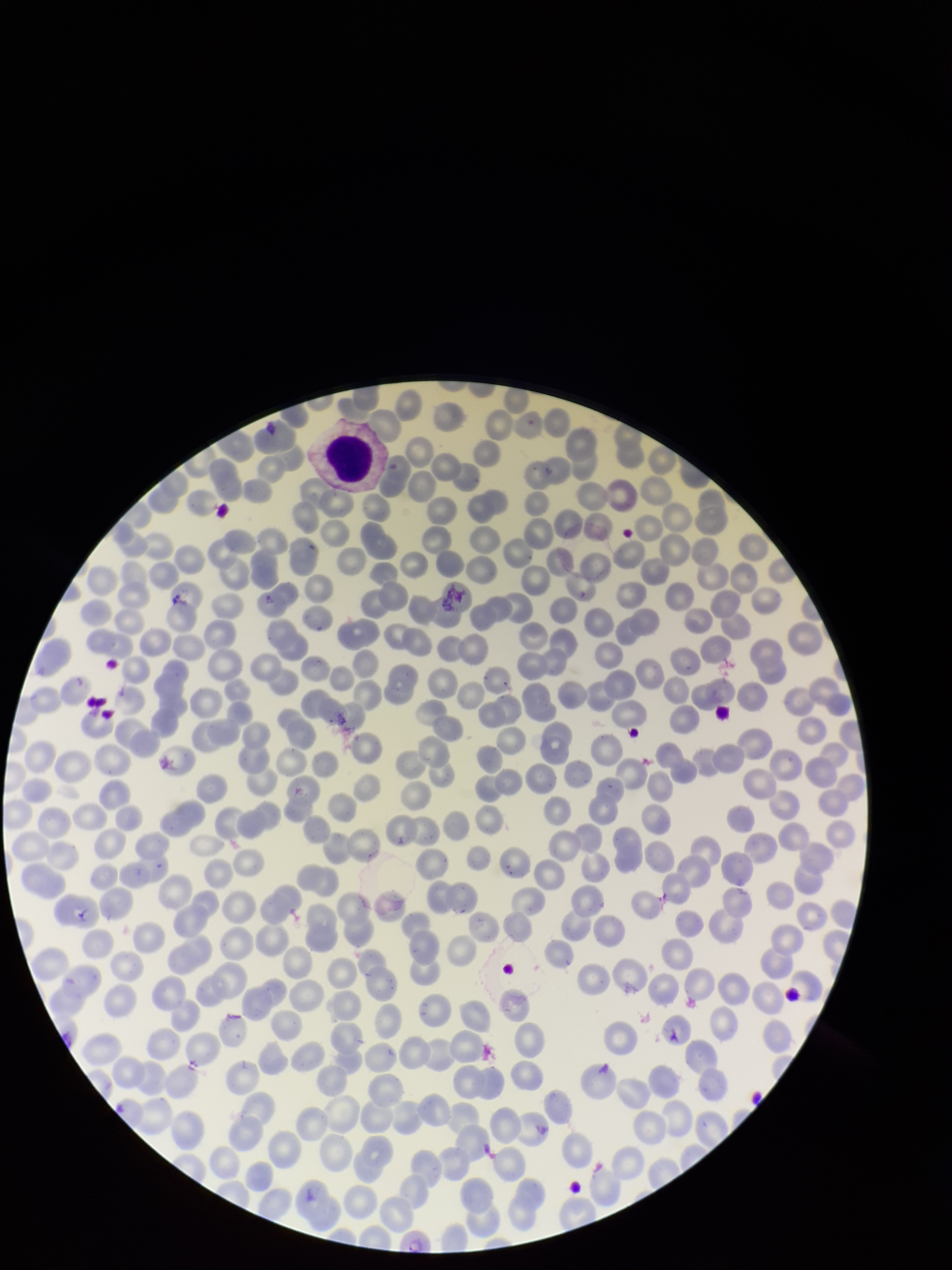

Summary:
  - Stain: Giemsa
  - Red blood cell count: 266
  - Field of view: single
  - Parasitized red blood cells: seen
  - Patient malaria status: positive
  - Species reported for this patient: Plasmodium vivax
  - Preparation: thin
  - Capture: smartphone photograph through the microscope eyepiece
  - Parasitized red blood cell count: 1
  - Image size: 952×1270 pixels